Report the malaria status of this cell.
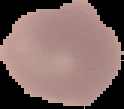

Uninfected.

Summary:
  - Preparation: thin blood smear
  - Image size: 124×109 pixels
  - Image type: cell region segmented out of the field of view; surrounding area masked to black